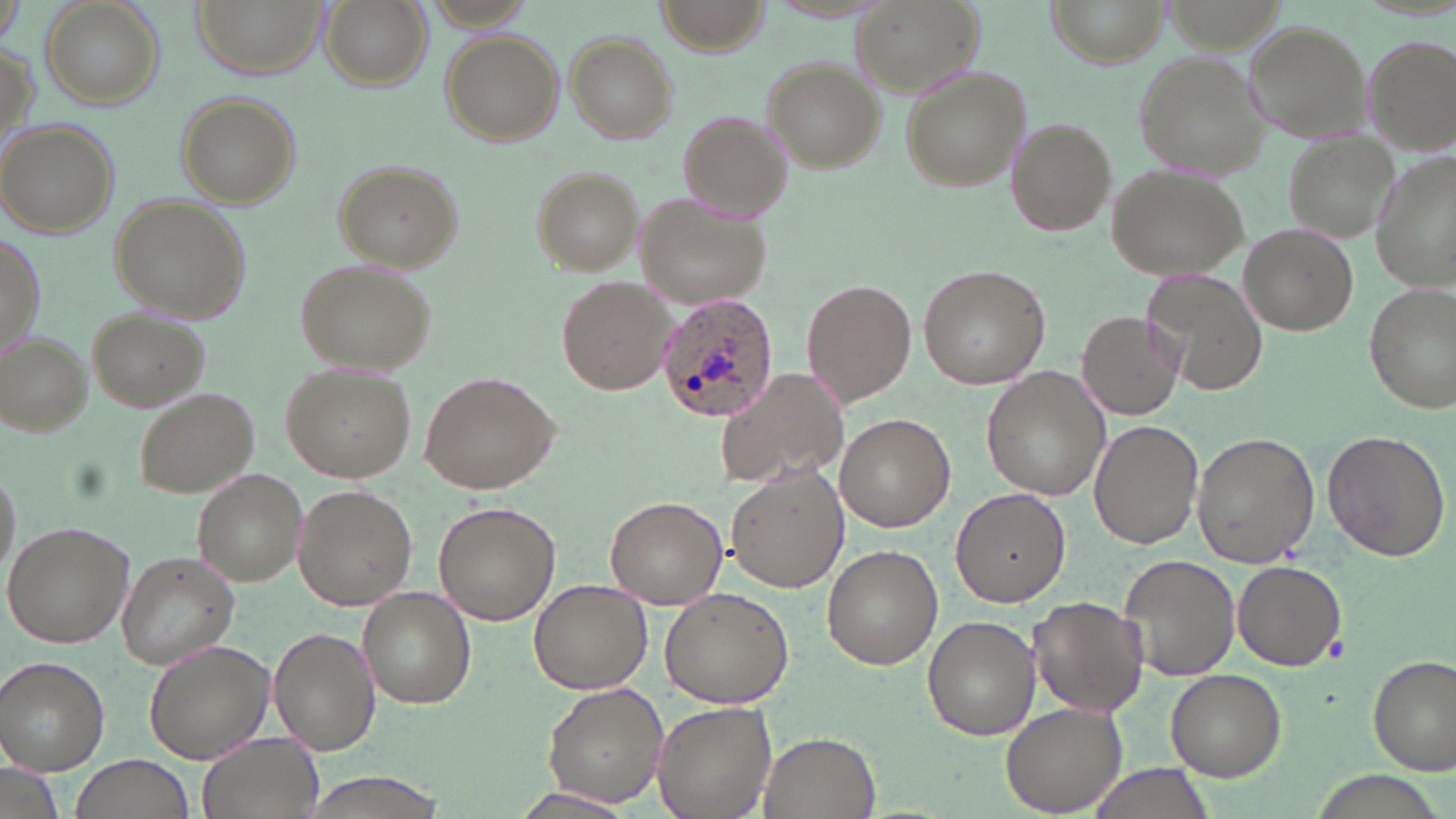

Approximate bounding boxes as [x1, y1, x2, y2] in pixels. Plasmodium ovale-infected red blood cell locations: [656, 291, 781, 425]. Uninfected red blood cell locations: [192, 0, 325, 77], [320, 0, 430, 91], [655, 0, 772, 55], [850, 0, 988, 99], [1047, 0, 1166, 69], [39, 1, 164, 111], [1, 2, 26, 48], [764, 3, 897, 22], [1242, 21, 1371, 140], [440, 30, 564, 146], [566, 30, 677, 141], [1363, 33, 1455, 152], [1134, 51, 1268, 177], [762, 57, 886, 171], [899, 65, 1031, 192], [177, 94, 300, 206], [678, 110, 794, 219], [1005, 118, 1115, 233], [1, 120, 117, 239], [1283, 130, 1400, 243], [1373, 150, 1456, 288], [334, 160, 460, 271], [529, 164, 647, 276], [1106, 164, 1249, 279], [638, 191, 771, 310], [106, 195, 252, 323], [1239, 223, 1359, 335], [0, 229, 44, 360], [296, 258, 438, 377], [919, 265, 1050, 390], [1145, 269, 1270, 396], [556, 276, 675, 396], [803, 280, 916, 405], [1363, 282, 1455, 413], [89, 307, 209, 412], [1075, 308, 1187, 422], [2, 332, 93, 434], [283, 368, 414, 480], [719, 368, 845, 489], [981, 368, 1107, 501], [422, 370, 559, 495], [133, 387, 258, 500], [836, 414, 955, 530], [1089, 420, 1202, 549], [1322, 430, 1452, 561], [1192, 431, 1320, 567], [0, 462, 19, 590], [727, 467, 849, 593], [192, 469, 308, 585], [295, 485, 416, 610], [950, 487, 1071, 607], [605, 493, 727, 608], [433, 502, 560, 625], [2, 522, 133, 648], [822, 544, 943, 669], [116, 551, 240, 668], [1119, 553, 1241, 680], [1232, 562, 1346, 670], [527, 579, 652, 694], [659, 587, 795, 708], [359, 588, 475, 709], [1028, 596, 1148, 716], [922, 614, 1039, 740], [269, 626, 379, 755], [143, 639, 276, 764], [1368, 654, 1454, 773], [1, 657, 109, 774], [1166, 670, 1284, 781], [543, 684, 668, 806], [652, 701, 775, 819], [1000, 701, 1128, 819], [758, 730, 880, 819], [197, 733, 324, 818], [74, 755, 192, 819], [1, 762, 60, 817], [1088, 763, 1210, 819], [1301, 769, 1444, 819], [502, 787, 640, 819]. Slide-level diagnosis: Plasmodium ovale. Thin blood film. Image is 1456×819 pixels. Optical microscopy. Single field of view. Captured at 1000x magnification. May-Grünwald-Giemsa-stained preparation.